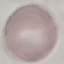

Summary:
  - Malaria status: uninfected
  - Capture: smartphone camera at the microscope eyepiece
  - Preparation: thin blood smear
  - Stain: Giemsa
  - Image type: automatically extracted cell patch, resized to 64 × 64 pixels